Identify the blood parasite species.
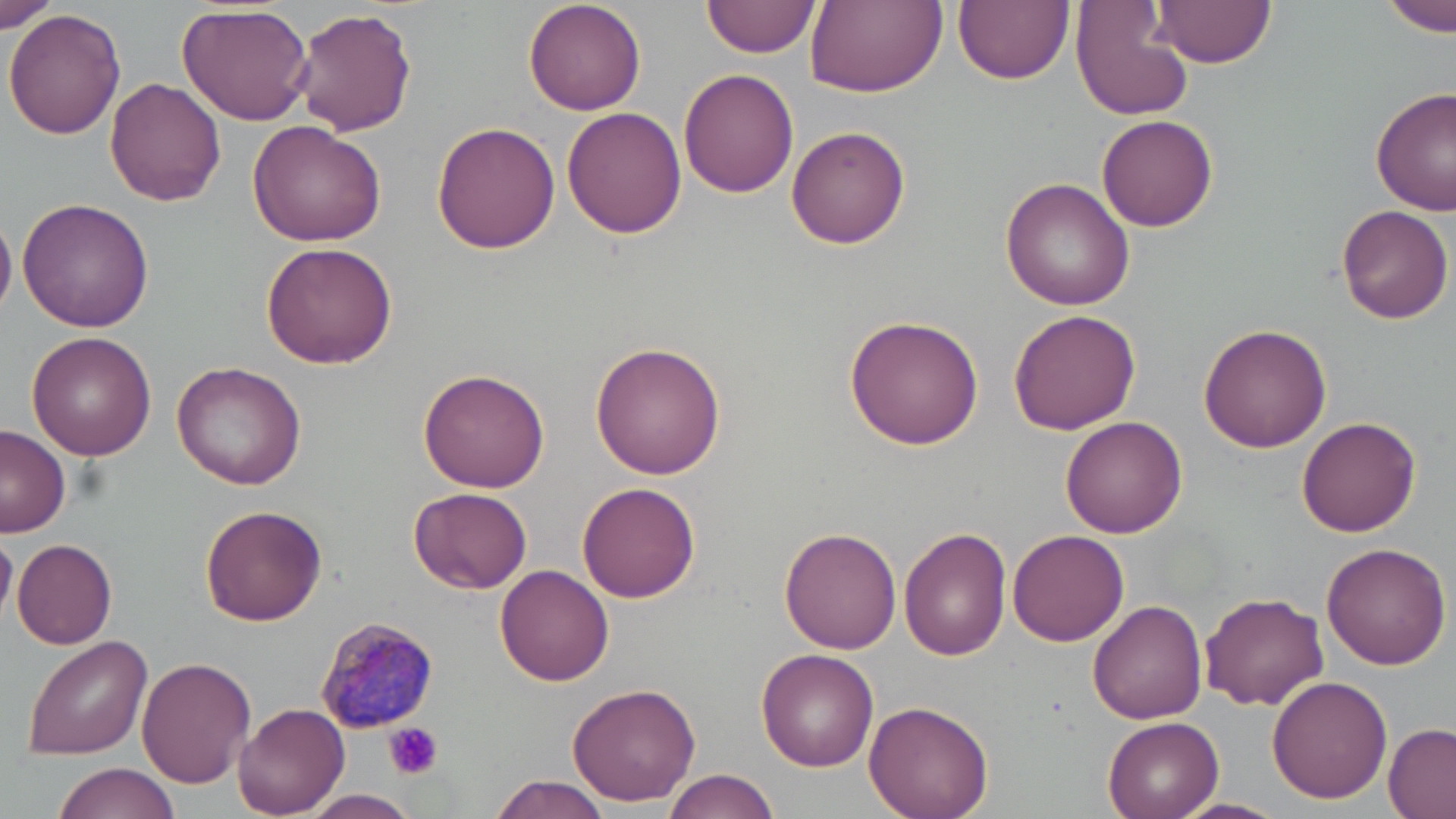
Plasmodium malariae.

Approximate bounding boxes as (x1, y1, x2, y2) in pixels. Platelet locations: (384, 722, 443, 780). Plasmodium malariae-infected red blood cell locations: (312, 612, 440, 734). Uninfected red blood cell locations: (523, 0, 648, 117), (704, 0, 820, 58), (954, 0, 1073, 86), (1149, 0, 1276, 68), (806, 1, 947, 99), (1378, 1, 1456, 36), (1071, 3, 1195, 120), (1, 4, 60, 34), (176, 4, 315, 128), (294, 7, 418, 137), (6, 9, 126, 140), (679, 67, 799, 197), (106, 77, 229, 208), (1371, 88, 1455, 215), (561, 108, 688, 240), (1097, 114, 1218, 231), (247, 120, 387, 247), (432, 121, 561, 254), (786, 123, 911, 249), (1000, 176, 1137, 309), (17, 198, 154, 331), (1336, 204, 1452, 324), (0, 211, 16, 321), (261, 241, 400, 368), (1007, 309, 1140, 435), (844, 314, 985, 450), (1198, 320, 1333, 451), (29, 332, 158, 462), (590, 341, 729, 479), (172, 361, 307, 490), (418, 370, 552, 494), (1296, 415, 1421, 537), (1060, 416, 1186, 538), (0, 424, 71, 538), (579, 482, 701, 604), (409, 487, 532, 596), (199, 505, 327, 625), (779, 528, 902, 655), (1007, 528, 1127, 645), (898, 529, 1012, 661), (0, 531, 17, 627), (12, 537, 119, 649), (1321, 541, 1451, 669), (495, 563, 614, 685), (1201, 592, 1330, 711), (1087, 599, 1207, 725), (20, 635, 153, 760), (755, 648, 876, 772), (136, 658, 256, 789), (1268, 675, 1392, 803), (566, 681, 700, 806), (866, 699, 995, 819), (234, 703, 349, 818), (1102, 716, 1223, 819), (1381, 721, 1456, 819), (53, 763, 181, 819), (662, 769, 779, 819), (487, 774, 613, 818), (305, 790, 420, 818), (1171, 798, 1291, 819). May-Grünwald-Giemsa-stained preparation. Optical microscopy. One field of a larger specimen. Captured at 1000x magnification. Thin blood film. Image is 1456×819 pixels.